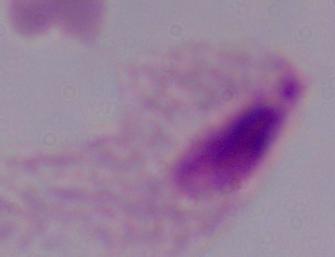

Summary:
  - Modality: photomicrograph
  - Identification: trichomonad
  - Magnification: 1000x